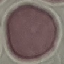
Summary:
  - Malaria status: uninfected
  - Image type: automatically extracted cell patch, resized to 64 × 64 pixels
  - Preparation: thin blood smear
  - Stain: Giemsa
  - Capture: smartphone through the microscope eyepiece